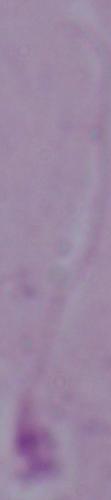 Micrograph. 1000x magnification. A Leishmania parasite is seen.